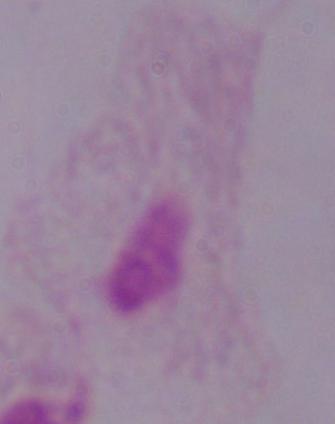
Photomicrograph. A trichomonad is seen. Captured at 1000x magnification.